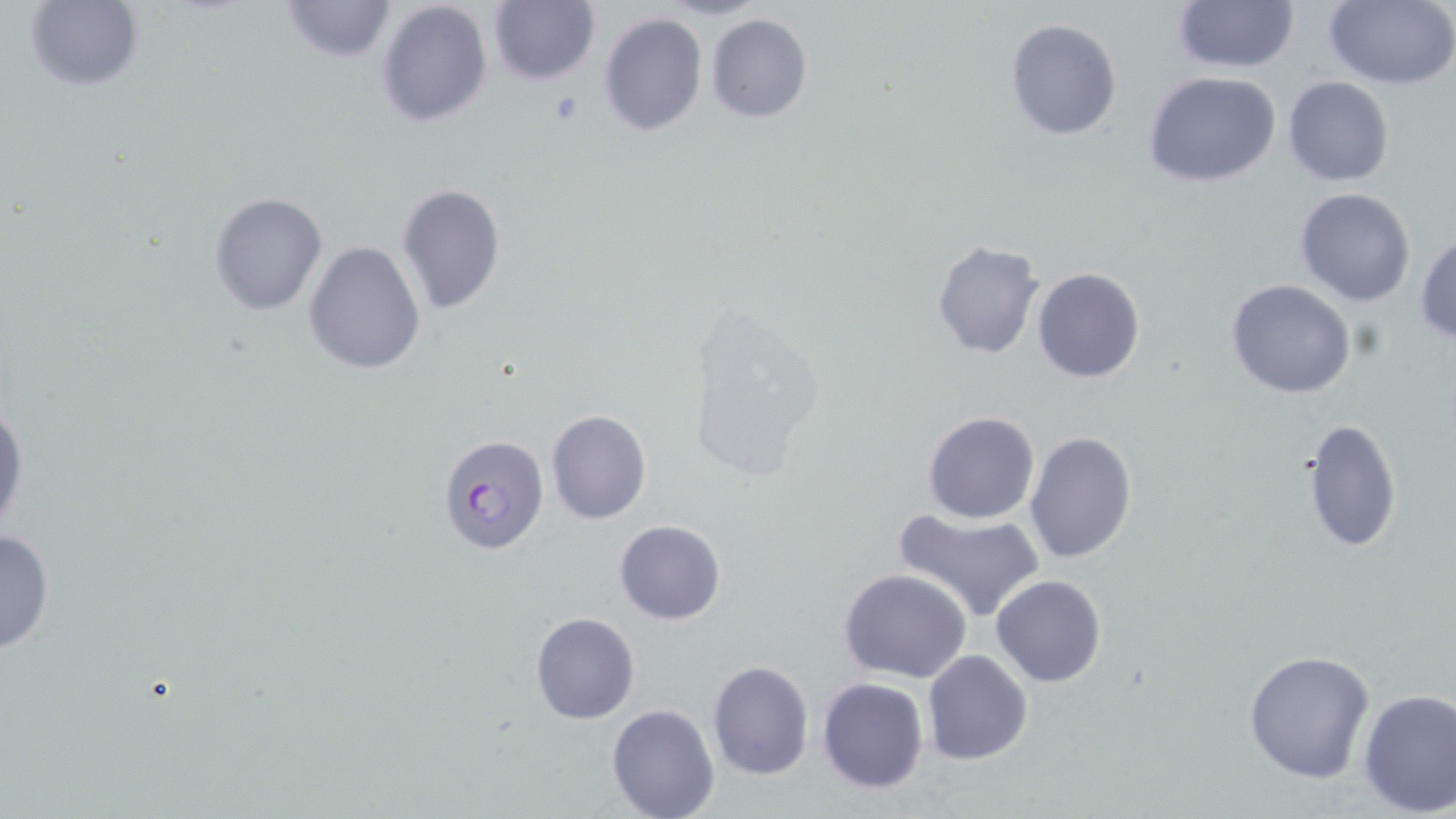

slide-level diagnosis = Plasmodium falciparum
image size = 1456×819 pixels
uninfected red blood cell locations = approximate bounding boxes as (x1,y1)-(x2,y2) corner pairs in pixels: (277,0)-(397,64), (1171,0)-(1298,72), (1326,0)-(1456,89), (25,1)-(143,91), (374,1)-(494,128), (488,1)-(598,86), (597,12)-(707,137), (706,14)-(813,123), (1005,18)-(1123,140), (1144,72)-(1280,188), (1282,76)-(1395,187), (395,184)-(507,315), (1295,188)-(1417,308), (208,192)-(327,317), (1414,231)-(1456,344), (303,239)-(425,374), (932,241)-(1045,360), (1032,267)-(1145,383), (1225,278)-(1356,399), (678,301)-(825,485), (0,400)-(28,540), (545,410)-(652,525), (922,410)-(1040,524), (1301,416)-(1402,555), (1024,431)-(1137,563), (892,506)-(1047,619), (614,520)-(727,625), (0,525)-(55,657), (838,567)-(971,683), (992,574)-(1107,689), (528,610)-(640,724), (1243,648)-(1375,784), (922,650)-(1033,764), (706,660)-(814,781), (816,676)-(930,794), (1357,687)-(1455,817), (607,703)-(719,819)
platelet locations = approximate bounding boxes as (x1,y1)-(x2,y2) corner pairs in pixels: (552,91)-(583,122)
modality = optical microscopy
field of view = one of a larger specimen
stain = May-Grünwald-Giemsa
Plasmodium falciparum-infected red blood cell locations = approximate bounding boxes as (x1,y1)-(x2,y2) corner pairs in pixels: (438,433)-(548,556)
preparation = thin blood smear
magnification = 1000x